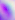

400x magnification. Micrograph. Toxoplasma gondii is shown.